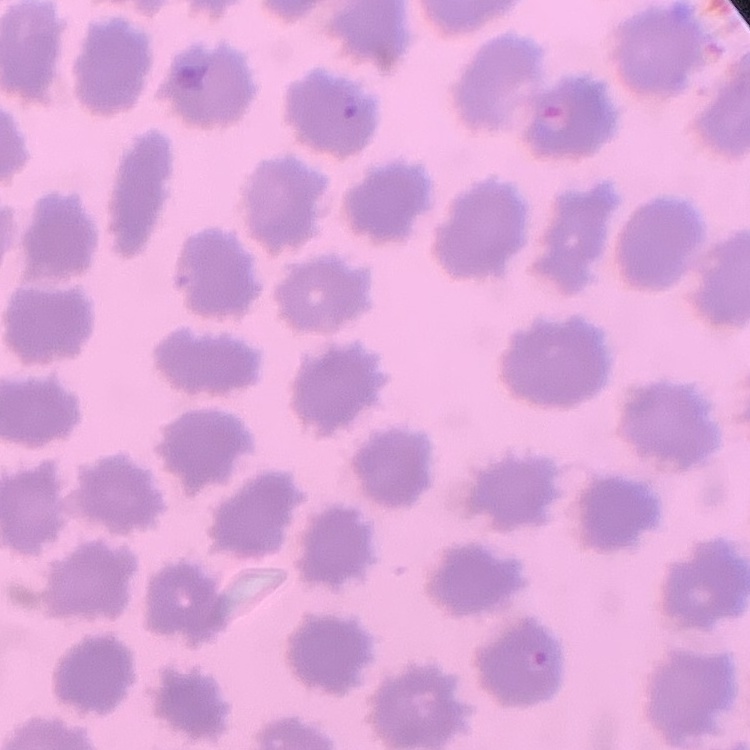

The red blood cells exhibit no rouleaux formation. Field's or Giemsa stain. Thin peripheral smear. Square crop of a larger photomicrograph.